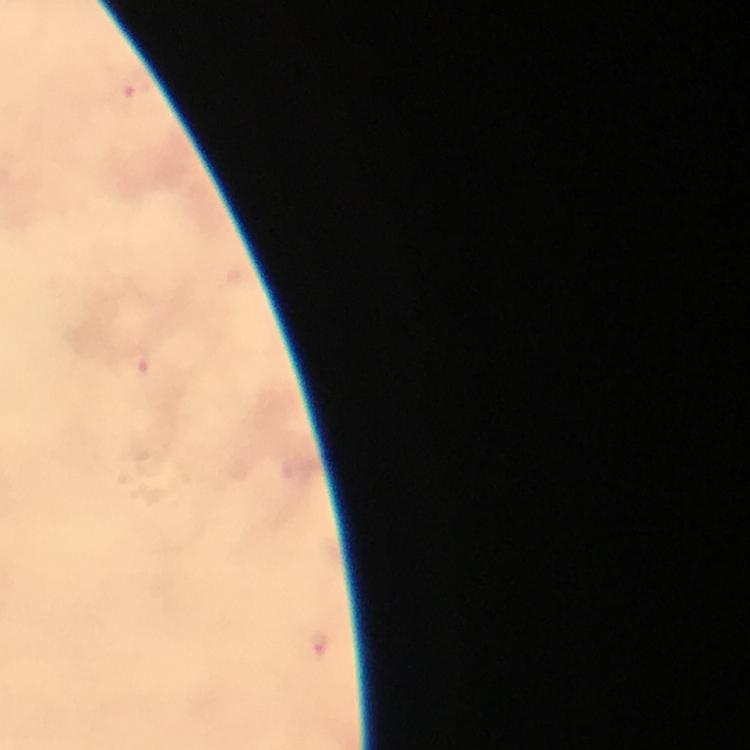
Approximate centers as {x, y} in pixels.
Summary:
  - Malaria parasite locations: {136, 88}, {135, 364}, {318, 643}
  - Immersion oil: used
  - Stain: Giemsa
  - Magnification: 100x
  - Context: from a malaria diagnostic workup
  - Cropped from: a single field of view
  - Preparation: thick smear
  - Image size: 750×750 pixels
  - Capture: smartphone photograph through a microscope